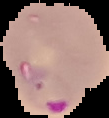
Summary:
  - Image type: cell region segmented out of the field of view; surrounding area masked to black
  - Preparation: thin blood film
  - Malaria status: parasitized
  - Image size: 109×118 pixels